Report the malaria status of this cell.
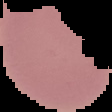

Uninfected.

image size = 112×112 pixels
preparation = thin blood smear
image type = cell region segmented out of the field of view; surrounding area masked to black